Classify this cell by malaria status.
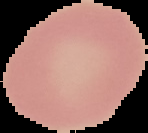
It is uninfected.

Summary:
  - Image type: cell region segmented out of the field of view; surrounding area masked to black
  - Image size: 148×133 pixels
  - Preparation: thin blood smear